State which parasite is depicted.
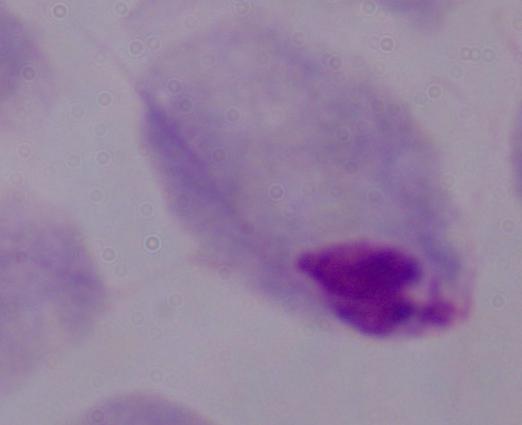
This is a trichomonad.

Summary:
  - Magnification: 1000x
  - Modality: photomicrograph